Name the parasite shown.
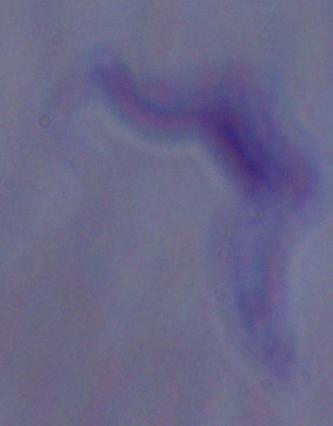

This is a trypanosome.

1000x magnification. Micrograph.